Report the malaria status of this cell.
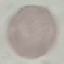
It is uninfected.

Thin blood film. Cell patch, automatically extracted from a larger field of view and resized to 64 × 64 pixels. Giemsa-stained preparation. Acquired by smartphone through the microscope eyepiece.